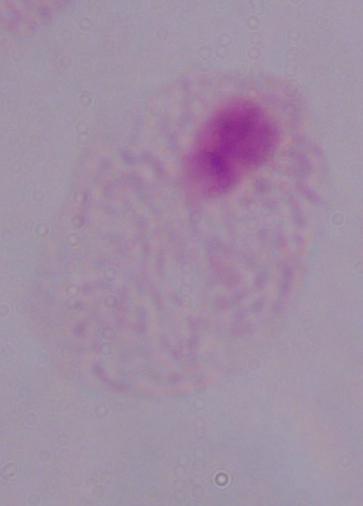
identification = trichomonad
magnification = 1000x
modality = photomicrograph